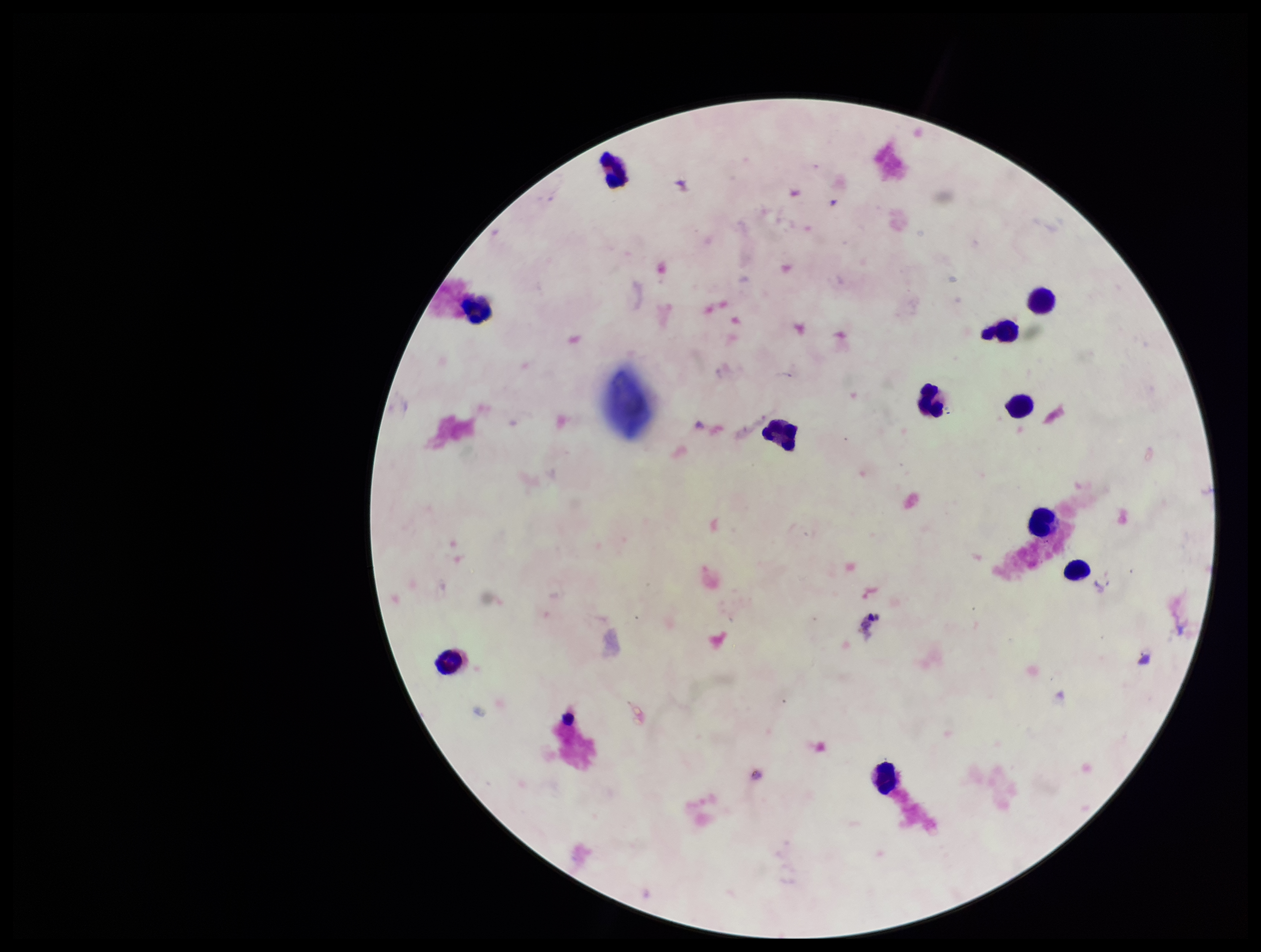 Patient malaria status: negative. Plasmodium parasites: none identified. Image is 1261×952 pixels. Parasite count: 0. Photographed through the microscope eyepiece with a smartphone camera. Stained with Giemsa. Preparation: thick blood smear. Leukocyte count: 11. Single field of view.